Assess this cell for malaria.
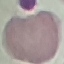
Uninfected.

capture = smartphone through the microscope eyepiece
stain = Giemsa
preparation = thin blood smear
image type = automatically extracted cell patch, resized to 64 × 64 pixels